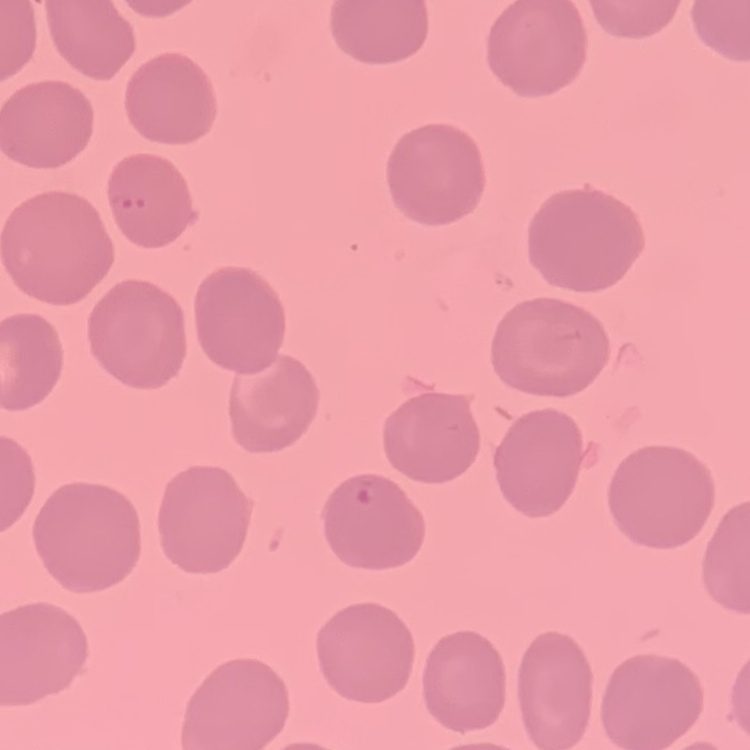
red_blood_cell_morphology: no rouleaux formation
preparation: thin blood smear
stain: Field's or Giemsa
image_type: square crop of a larger photomicrograph